Assess this cell for malaria.
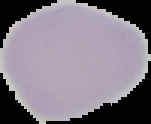

It is uninfected.

image type = segmented cell region on a black background
preparation = thin blood film
image size = 151×124 pixels